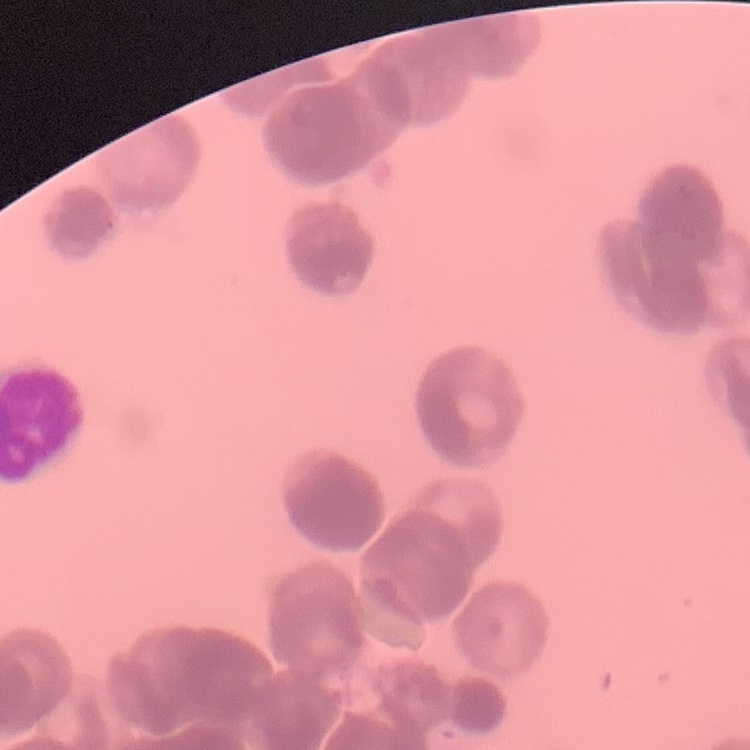

red blood cell morphology = rouleaux formation
image type = one tile cut from a larger photomicrograph
stain = Field's or Giemsa
preparation = thin peripheral smear